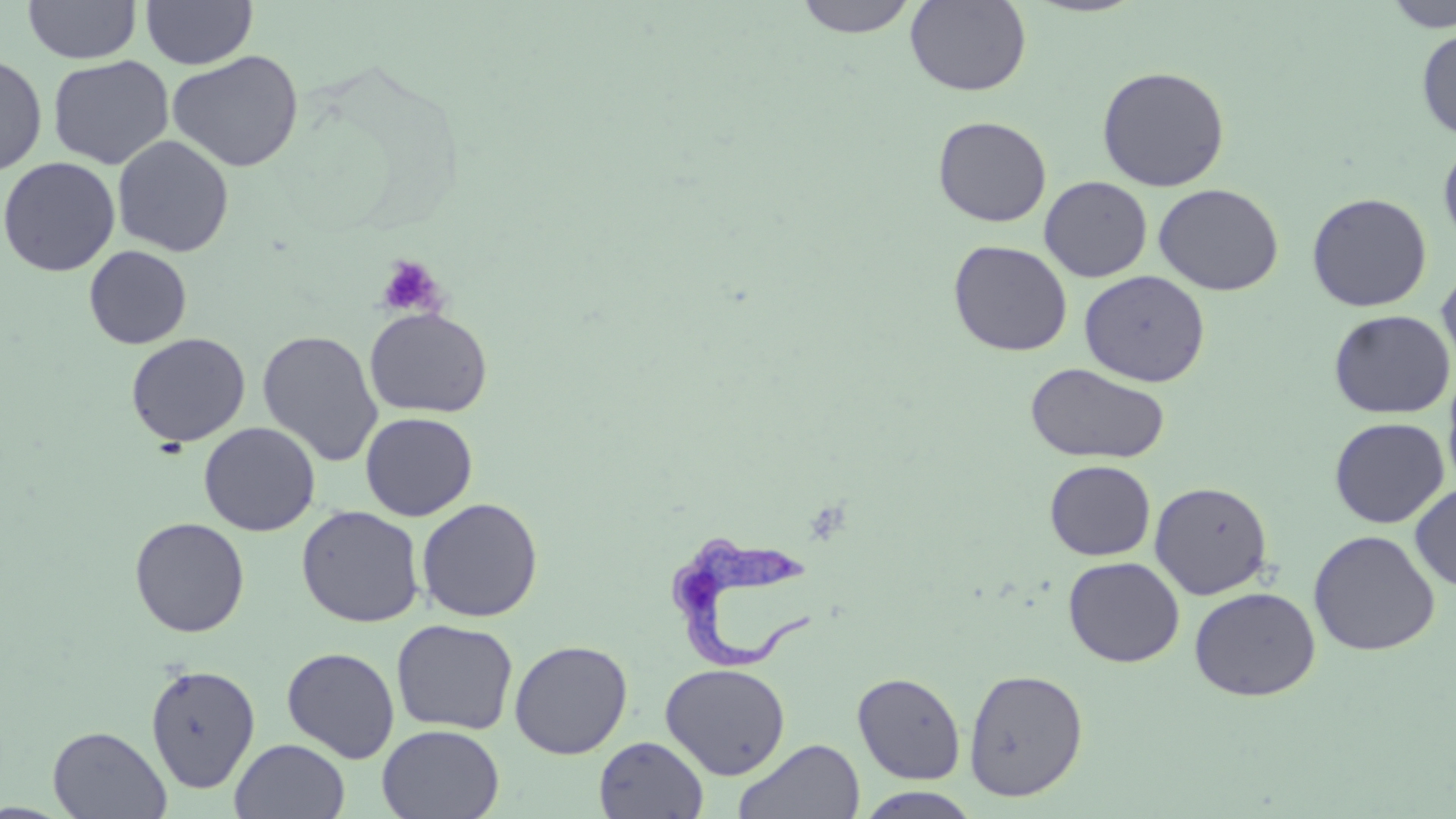

Summary:
  - Coordinate format: approximate bounding boxes as (x1, y1, x2, y2) in pixels
  - Platelet locations: (376, 255, 445, 318)
  - Uninfected red blood cell locations: (24, 0, 141, 64), (141, 0, 257, 69), (794, 0, 919, 38), (905, 0, 1031, 96), (1383, 0, 1456, 32), (1416, 28, 1456, 141), (167, 50, 304, 172), (0, 54, 48, 177), (48, 55, 174, 170), (1096, 65, 1231, 192), (933, 115, 1052, 227), (113, 135, 234, 257), (1438, 138, 1456, 250), (0, 156, 121, 276), (1039, 176, 1152, 282), (1153, 183, 1284, 296), (1306, 192, 1432, 312), (948, 240, 1072, 356), (84, 245, 193, 349), (1437, 264, 1456, 378), (1079, 270, 1210, 387), (364, 307, 493, 418), (1327, 309, 1455, 418), (257, 330, 383, 467), (125, 332, 250, 448), (1024, 363, 1171, 465), (1443, 366, 1456, 493), (360, 411, 478, 521), (1329, 417, 1450, 529), (198, 421, 321, 536), (1045, 460, 1155, 560), (1149, 481, 1273, 600), (1410, 483, 1456, 592), (416, 497, 544, 623), (296, 505, 425, 628), (129, 516, 250, 637), (1308, 529, 1440, 656), (1063, 556, 1185, 668), (1189, 586, 1321, 701), (391, 618, 518, 736), (509, 639, 633, 759), (281, 647, 400, 763), (660, 662, 790, 779), (145, 663, 261, 794), (963, 668, 1088, 802), (852, 672, 966, 784), (376, 724, 505, 819), (47, 725, 172, 818), (594, 735, 708, 819), (230, 738, 350, 819), (733, 738, 866, 819), (856, 787, 983, 818)
  - Trypanosoma brucei locations: (669, 527, 822, 670)
  - Slide-level diagnosis: Trypanosoma brucei
  - Modality: light microscopy
  - Image size: 1456×819 pixels
  - Magnification: 1000x
  - Stain: May-Grünwald-Giemsa
  - Preparation: thin blood film
  - Field of view: one of a larger specimen